Assess this cell for malaria.
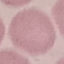
It is uninfected.

Thin smear of blood. Automatically extracted cell patch, resized to 64 × 64 pixels. Photographed with a smartphone camera at the microscope eyepiece. Giemsa-stained preparation.